State which cell type is depicted.
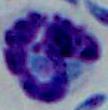

A leukocyte.

1000x magnification. Micrograph.